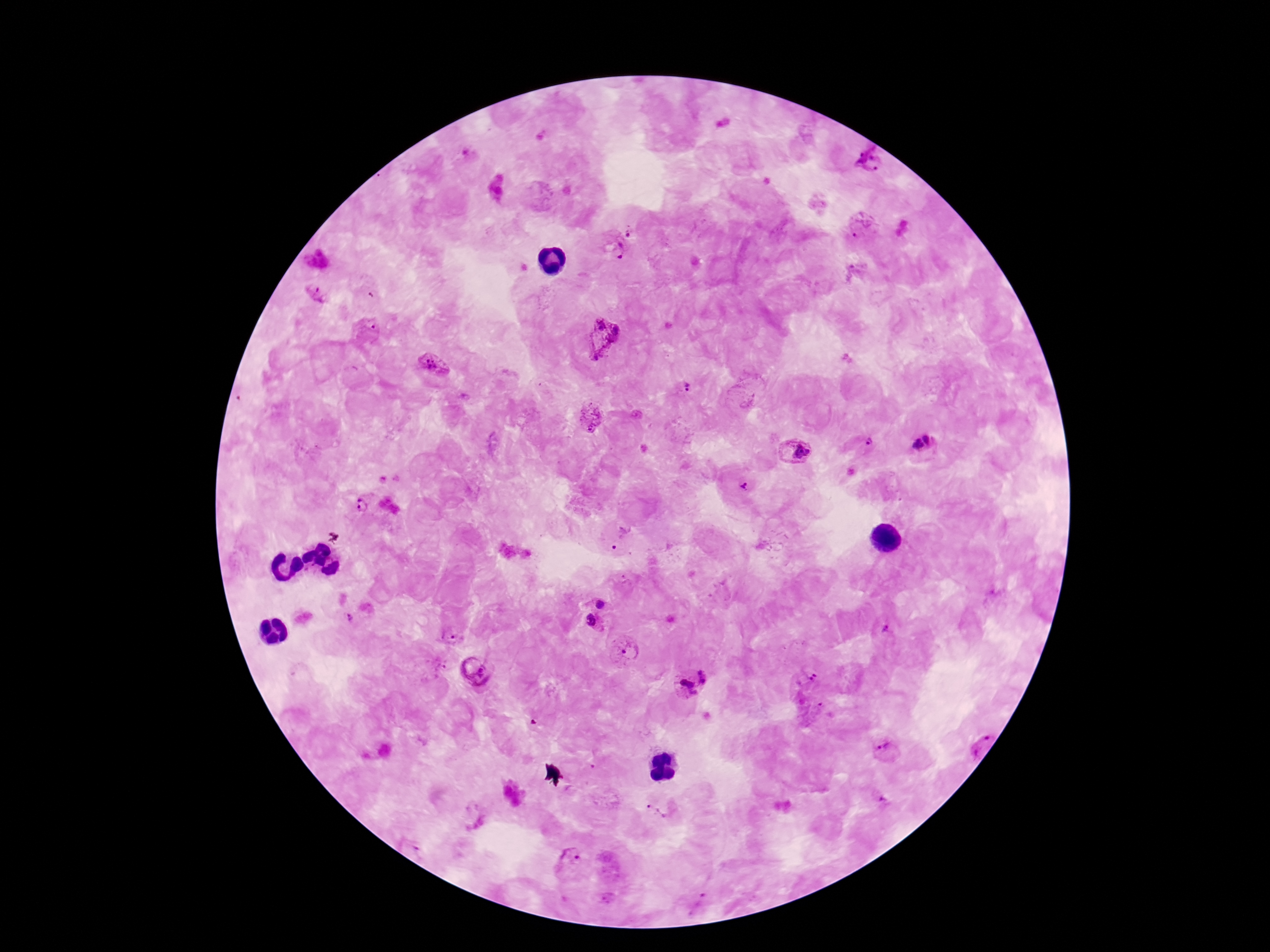

capture = smartphone camera through the microscope eyepiece
magnification = 100x
patient malaria status = infected
preparation = thick blood film
stain = Giemsa
Plasmodium parasite locations = approximate centers as {x, y} in pixels: {869, 162}, {637, 229}, {861, 229}, {617, 252}, {314, 296}, {369, 333}, {602, 336}, {435, 366}, {689, 389}, {590, 417}, {866, 443}, {923, 444}, {794, 451}, {743, 487}, {357, 505}, {621, 539}, {601, 599}, {350, 615}, {595, 624}, {886, 629}, {449, 636}, {623, 653}, {436, 667}, {477, 673}, {808, 677}, {692, 681}, {810, 709}, {977, 741}, {884, 749}, {655, 810}, {572, 862}, {697, 897}
field of view = single
image size = 1270×952 pixels